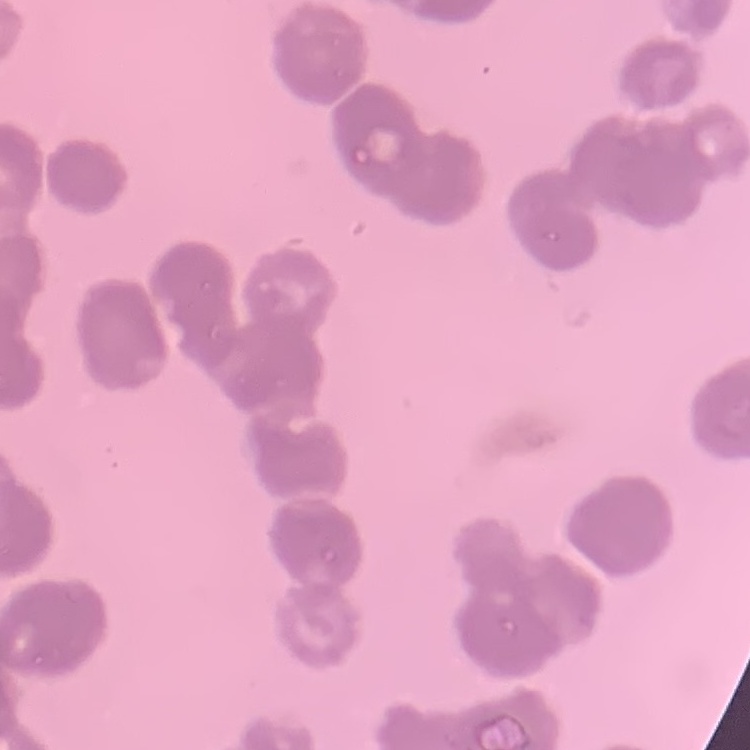
erythrocyte morphology = rouleaux formation
preparation = thin blood smear
image type = square crop of a larger photomicrograph
stain = Field's or Giemsa